State which parasite is depicted.
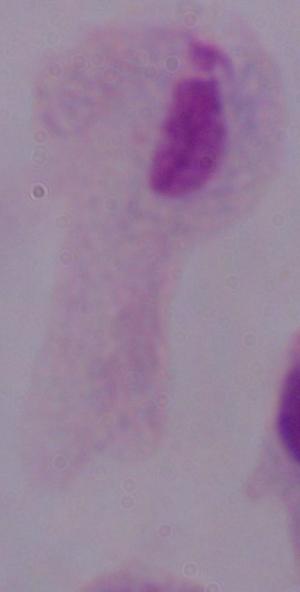
A trichomonad.

Photomicrograph. 1000x magnification.